Identify the blood parasite species.
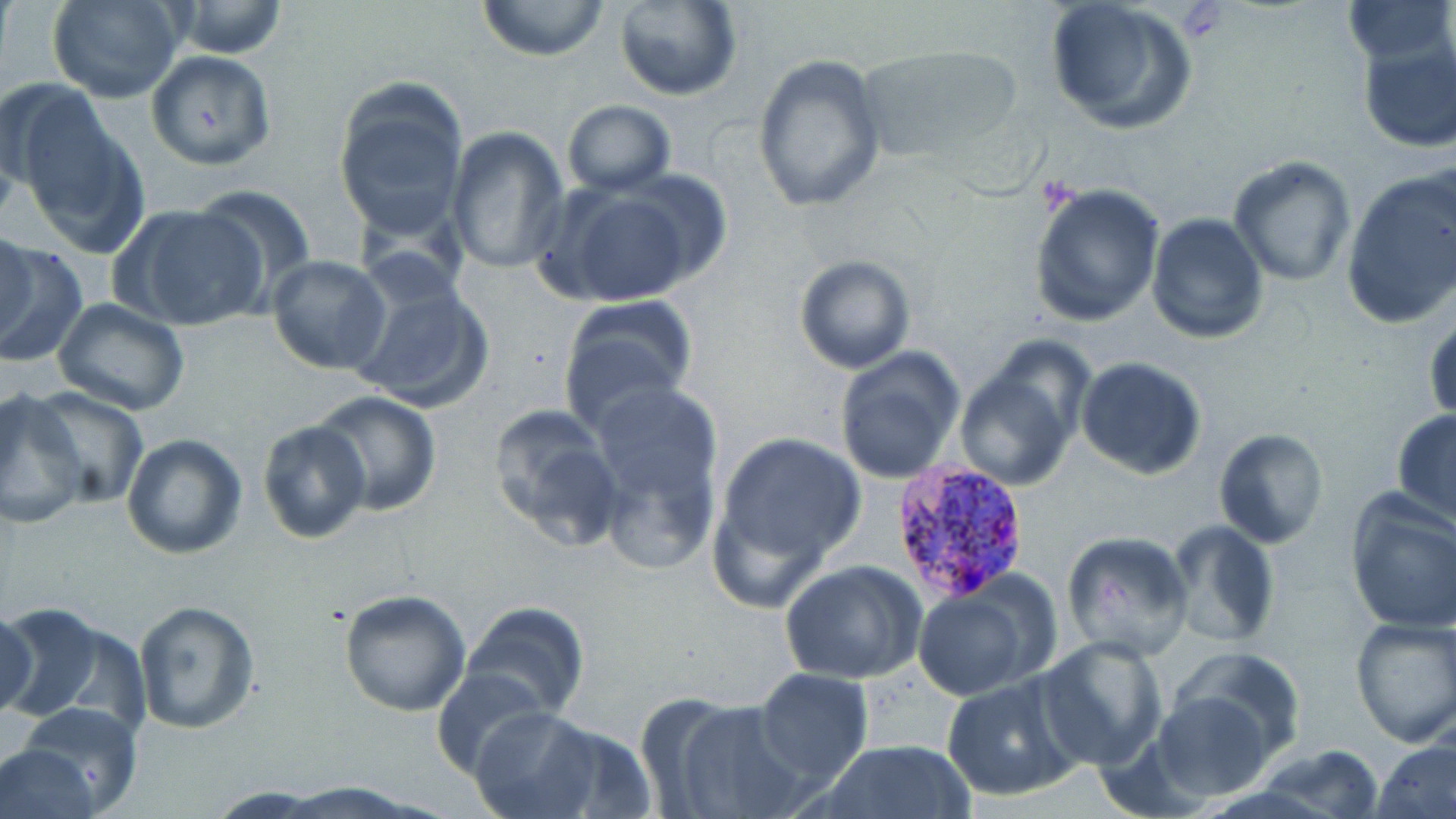
Plasmodium vivax.

Approximate bounding boxes as named x1/y1/x2/y2 corners in pixels. Uninfected red blood cell locations: (x1=48, y1=0, x2=187, y2=104), (x1=475, y1=0, x2=612, y2=60), (x1=1044, y1=0, x2=1196, y2=134), (x1=1341, y1=0, x2=1455, y2=69), (x1=172, y1=1, x2=289, y2=58), (x1=612, y1=1, x2=743, y2=102), (x1=1356, y1=32, x2=1456, y2=152), (x1=853, y1=42, x2=1023, y2=165), (x1=145, y1=50, x2=276, y2=169), (x1=753, y1=54, x2=886, y2=212), (x1=333, y1=81, x2=471, y2=234), (x1=8, y1=86, x2=143, y2=247), (x1=562, y1=100, x2=676, y2=197), (x1=446, y1=127, x2=568, y2=273), (x1=1229, y1=154, x2=1359, y2=287), (x1=1342, y1=170, x2=1456, y2=328), (x1=1028, y1=181, x2=1166, y2=326), (x1=549, y1=182, x2=706, y2=307), (x1=190, y1=184, x2=319, y2=306), (x1=123, y1=203, x2=268, y2=333), (x1=1146, y1=212, x2=1269, y2=343), (x1=1, y1=230, x2=35, y2=350), (x1=0, y1=244, x2=88, y2=366), (x1=267, y1=254, x2=392, y2=374), (x1=794, y1=254, x2=917, y2=374), (x1=345, y1=266, x2=496, y2=417), (x1=555, y1=294, x2=698, y2=432), (x1=52, y1=298, x2=192, y2=418), (x1=1426, y1=311, x2=1456, y2=422), (x1=833, y1=346, x2=965, y2=484), (x1=1075, y1=357, x2=1207, y2=480), (x1=954, y1=369, x2=1077, y2=490), (x1=587, y1=379, x2=725, y2=567), (x1=28, y1=385, x2=148, y2=508), (x1=0, y1=390, x2=89, y2=529), (x1=314, y1=391, x2=442, y2=516), (x1=485, y1=401, x2=624, y2=553), (x1=1391, y1=409, x2=1456, y2=526), (x1=256, y1=418, x2=372, y2=544), (x1=1212, y1=427, x2=1328, y2=548), (x1=712, y1=429, x2=865, y2=581), (x1=121, y1=432, x2=248, y2=559), (x1=1195, y1=451, x2=1320, y2=621), (x1=1344, y1=493, x2=1456, y2=635), (x1=1163, y1=521, x2=1280, y2=649), (x1=1060, y1=530, x2=1195, y2=662), (x1=778, y1=560, x2=927, y2=683), (x1=912, y1=580, x2=1049, y2=701), (x1=338, y1=589, x2=471, y2=716), (x1=133, y1=600, x2=260, y2=732), (x1=461, y1=601, x2=590, y2=720), (x1=0, y1=603, x2=145, y2=733), (x1=0, y1=604, x2=40, y2=724), (x1=1349, y1=616, x2=1456, y2=748), (x1=1036, y1=637, x2=1168, y2=769), (x1=1167, y1=647, x2=1307, y2=764), (x1=432, y1=666, x2=550, y2=779), (x1=753, y1=668, x2=873, y2=787), (x1=939, y1=674, x2=1081, y2=803), (x1=1151, y1=689, x2=1277, y2=802), (x1=666, y1=698, x2=810, y2=819), (x1=13, y1=702, x2=144, y2=818), (x1=468, y1=707, x2=601, y2=816), (x1=1372, y1=737, x2=1456, y2=819), (x1=818, y1=740, x2=974, y2=819), (x1=1258, y1=742, x2=1383, y2=819), (x1=0, y1=743, x2=101, y2=819), (x1=271, y1=783, x2=430, y2=816). Plasmodium vivax-infected red blood cell locations: (x1=890, y1=459, x2=1030, y2=601). Platelet locations: (x1=1177, y1=4, x2=1228, y2=39). Light microscopy. Thin blood film. May-Grünwald-Giemsa-stained preparation. Image is 1456×819 pixels. One field of a larger specimen. Captured at 1000x magnification.